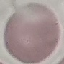
Malaria status: uninfected. Thin blood smear. Photographed with a smartphone camera at the microscope eyepiece. Giemsa-stained preparation. Automatically extracted cell patch, resized to 64 × 64 pixels.